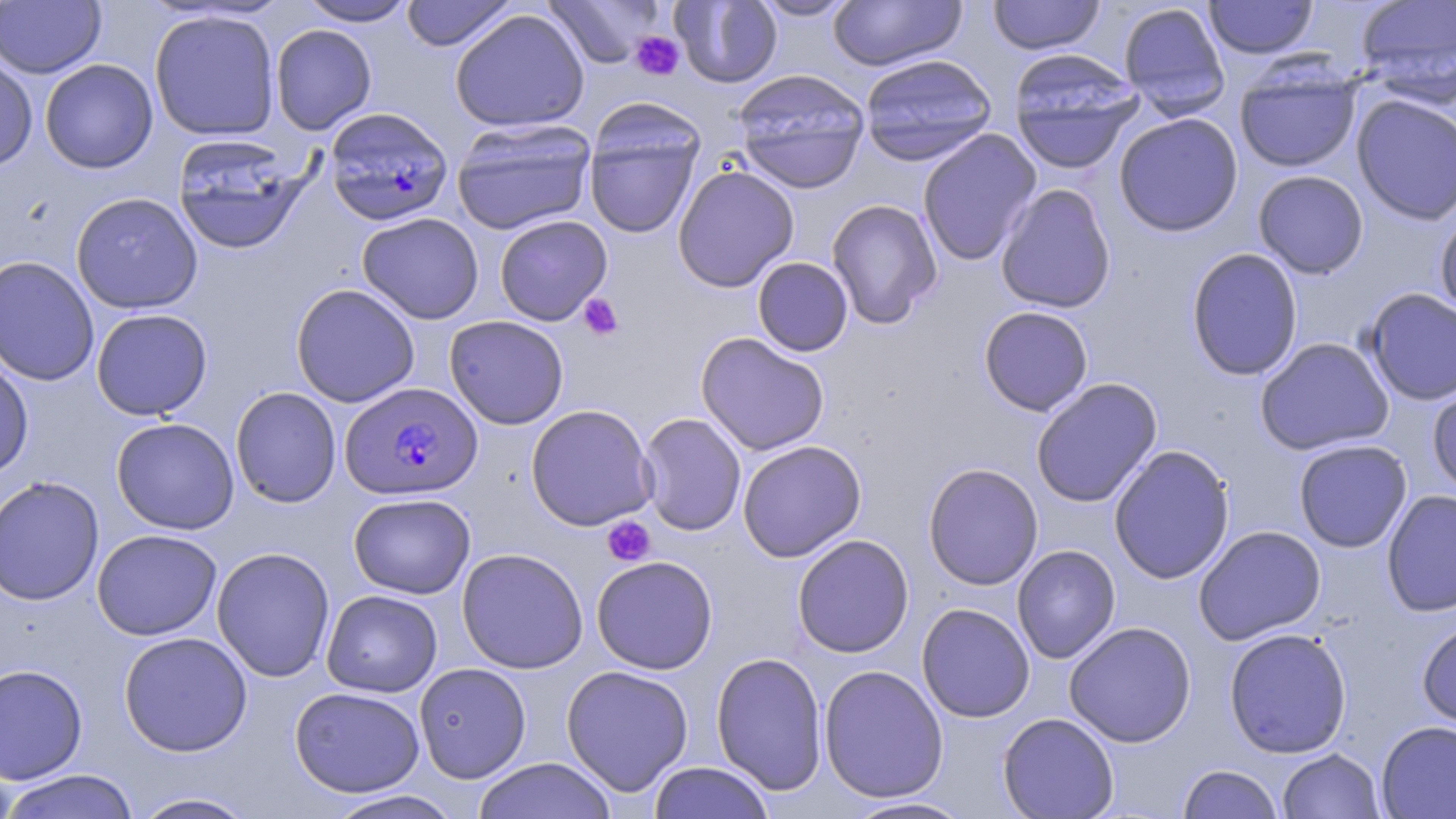

slide-level diagnosis = Plasmodium falciparum
platelet locations = approximate bounding boxes as [x1, y1, x2, y2] in pixels: [630, 31, 684, 80], [578, 294, 624, 341], [602, 516, 656, 567]
stain = May-Grünwald-Giemsa
magnification = 1000x
uninfected red blood cell locations = approximate bounding boxes as [x1, y1, x2, y2] in pixels: [297, 0, 418, 26], [400, 0, 517, 51], [541, 0, 666, 68], [670, 0, 783, 88], [751, 0, 860, 21], [988, 0, 1105, 55], [1204, 0, 1319, 59], [1354, 0, 1456, 104], [1, 1, 106, 78], [828, 1, 966, 71], [1117, 2, 1230, 117], [449, 8, 590, 133], [149, 9, 281, 141], [270, 24, 377, 135], [1008, 50, 1144, 173], [0, 53, 38, 172], [858, 53, 997, 165], [40, 59, 158, 173], [1234, 63, 1361, 173], [732, 68, 870, 194], [1351, 94, 1456, 226], [1114, 113, 1243, 237], [583, 115, 705, 241], [451, 119, 597, 234], [917, 129, 1042, 266], [170, 134, 310, 255], [672, 165, 799, 292], [1253, 170, 1369, 279], [996, 183, 1116, 314], [70, 192, 203, 314], [825, 198, 943, 329], [1435, 210, 1456, 323], [356, 212, 484, 324], [494, 214, 613, 326], [1186, 247, 1304, 381], [0, 255, 100, 387], [752, 257, 853, 356], [290, 283, 421, 407], [1363, 287, 1456, 405], [978, 306, 1094, 416], [91, 308, 213, 421], [444, 315, 569, 430], [695, 332, 830, 456], [1255, 337, 1395, 455], [0, 354, 34, 481], [1030, 378, 1163, 508], [1428, 382, 1456, 497], [230, 386, 342, 508], [525, 404, 657, 531], [638, 413, 747, 536], [111, 417, 239, 535], [1293, 439, 1412, 553], [737, 440, 866, 562], [1108, 444, 1235, 584], [922, 462, 1044, 590], [0, 475, 105, 606], [1381, 489, 1456, 617], [348, 493, 476, 598], [1193, 525, 1326, 645], [92, 528, 222, 641], [791, 534, 914, 658], [1011, 544, 1121, 664], [211, 547, 336, 682], [457, 547, 589, 674], [591, 555, 718, 674], [321, 589, 442, 697], [916, 603, 1035, 723], [1416, 619, 1456, 732], [1064, 621, 1197, 747], [1223, 627, 1352, 758], [118, 631, 253, 757], [711, 650, 828, 796], [413, 662, 531, 783], [0, 663, 88, 785], [819, 664, 948, 803], [561, 665, 694, 796], [289, 686, 426, 797], [997, 712, 1119, 818], [1375, 720, 1456, 818], [1277, 748, 1385, 819], [473, 758, 617, 819], [647, 762, 776, 818], [1177, 764, 1284, 819], [0, 770, 141, 819], [322, 790, 465, 819], [129, 791, 261, 819], [843, 795, 976, 818]
image size = 1456×819 pixels
modality = light microscopy
Plasmodium falciparum-infected red blood cell locations = approximate bounding boxes as [x1, y1, x2, y2] in pixels: [324, 106, 454, 226], [340, 381, 482, 500]
field of view = single
preparation = thin blood film